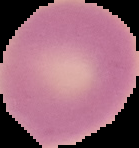

Malaria status: uninfected. From a thin blood film. Cell region segmented out of the field of view; the surrounding area is masked to black. Image is 139×148 pixels.